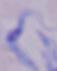 Captured at 1000x magnification. A trypanosome is shown. Micrograph.